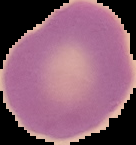
Malaria status: uninfected. From a thin blood film. Image is 136×145 pixels. Cell region segmented out of the field of view; the surrounding area is masked to black.